Locate every malaria parasite.
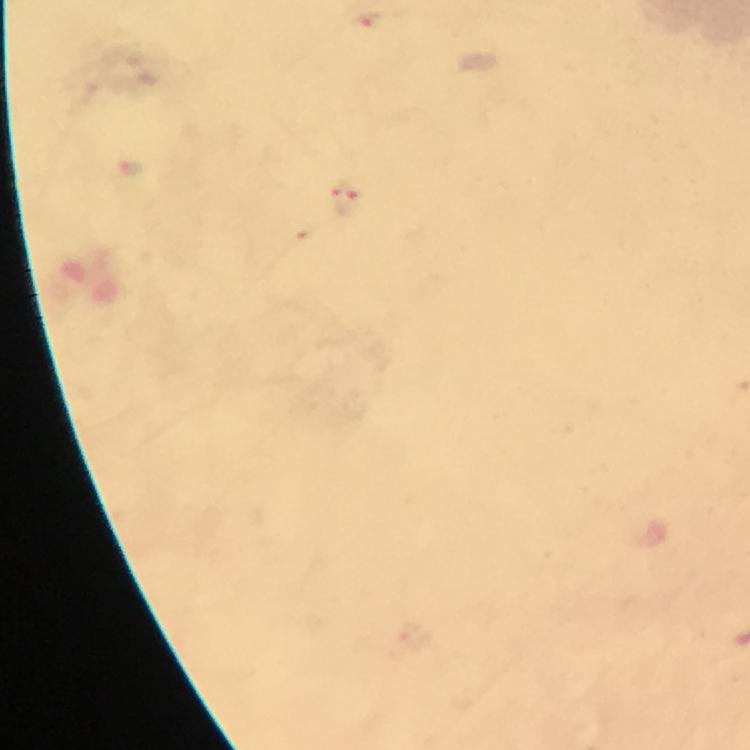

Approximate centers as [x, y] in pixels.
Malaria parasites: [368, 18], [344, 198].

Summary:
  - Capture: smartphone camera through the microscope
  - Stain: Giemsa
  - Cropped from: one field of view
  - Preparation: thick smear
  - Immersion oil: applied
  - Magnification: 100x
  - Image size: 750×750 pixels
  - Context: from a diagnostic examination for malaria